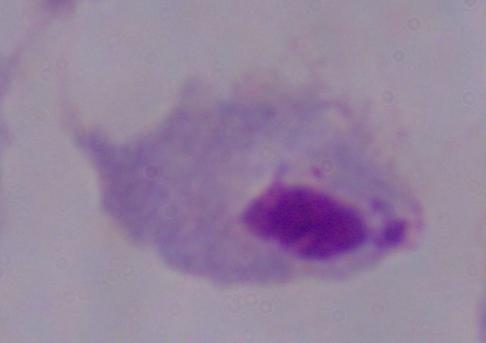
magnification: 1000x
identification: trichomonad
modality: photomicrograph